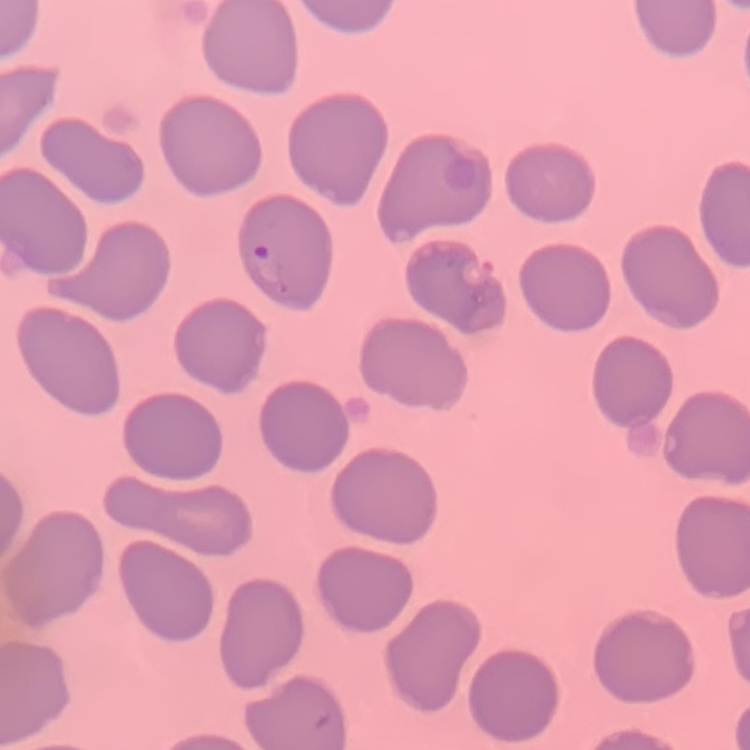
red blood cell morphology = no rouleaux formation
stain = Field's or Giemsa
preparation = thin blood film
image type = one tile cut from a larger photomicrograph